Identify the parasite.
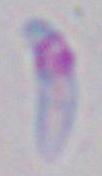

This is Toxoplasma gondii.

magnification = 1000x
modality = micrograph